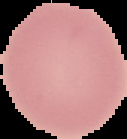
Summary:
  - Image type: cell region segmented out of the field of view; surrounding area masked to black
  - Malaria status: uninfected
  - Image size: 127×139 pixels
  - Preparation: thin blood film